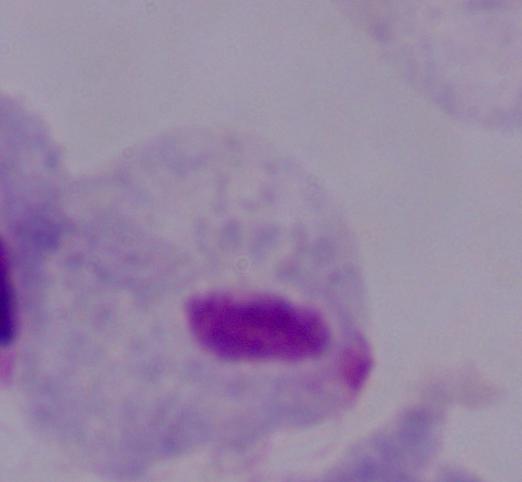

Summary:
  - Modality: photomicrograph
  - Magnification: 1000x
  - Identification: trichomonad